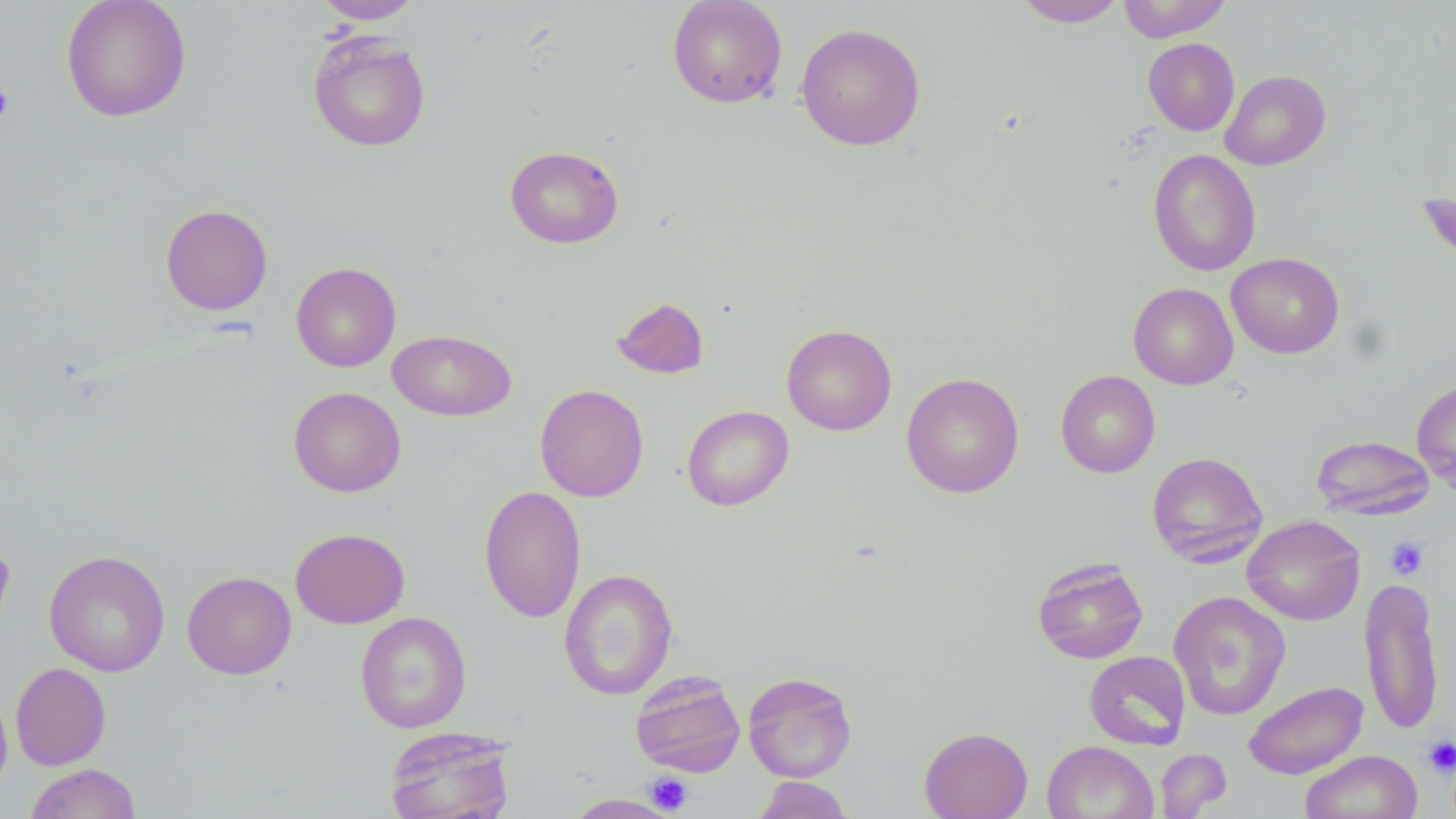
{
  "slide_level_diagnosis": "no evidence of blood parasites",
  "stain": "May-Grünwald-Giemsa",
  "preparation": "thin blood film",
  "field_of_view": "single",
  "magnification": "1000x",
  "platelet_locations": "approximate bounding boxes as (x1, y1, x2, y2) in pixels: (0, 82, 14, 124), (1385, 537, 1428, 580), (1423, 736, 1456, 777), (645, 772, 693, 815)",
  "image_size": "1456×819 pixels",
  "uninfected_red_blood_cell_locations": "approximate bounding boxes as (x1, y1, x2, y2) in pixels: (60, 0, 192, 123), (312, 0, 425, 23), (667, 0, 788, 109), (1013, 0, 1127, 27), (1117, 0, 1233, 42), (795, 22, 926, 151), (307, 31, 431, 152), (1143, 37, 1240, 136), (1220, 70, 1331, 171), (504, 145, 624, 249), (1148, 148, 1261, 277), (1417, 190, 1456, 270), (160, 203, 273, 316), (1226, 252, 1345, 359), (290, 262, 401, 372), (1128, 282, 1238, 389), (611, 296, 709, 380), (781, 323, 897, 435), (387, 328, 517, 422), (1056, 370, 1160, 478), (901, 372, 1024, 498), (1411, 380, 1456, 496), (534, 384, 649, 502), (288, 386, 406, 497), (682, 405, 794, 511), (1310, 434, 1435, 520), (1147, 451, 1268, 568), (478, 485, 586, 623), (1242, 515, 1365, 625), (290, 527, 410, 629), (0, 536, 15, 637), (44, 549, 170, 677), (1032, 557, 1148, 664), (558, 569, 678, 700), (182, 571, 297, 679), (1359, 575, 1445, 736), (1169, 591, 1291, 720), (355, 611, 472, 733), (1084, 651, 1191, 750), (10, 662, 111, 770), (630, 669, 746, 777), (743, 671, 858, 782), (1243, 680, 1367, 779), (0, 686, 12, 799), (384, 726, 516, 819), (919, 726, 1033, 819), (1042, 740, 1158, 819), (1155, 748, 1232, 818), (1301, 749, 1423, 819), (25, 763, 142, 819), (646, 772, 692, 814), (752, 776, 854, 818), (563, 793, 681, 818)",
  "modality": "light microscopy"
}